Identify the parasite.
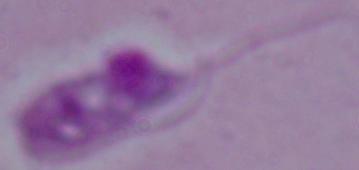

Leishmania.

modality: photomicrograph
magnification: 1000x